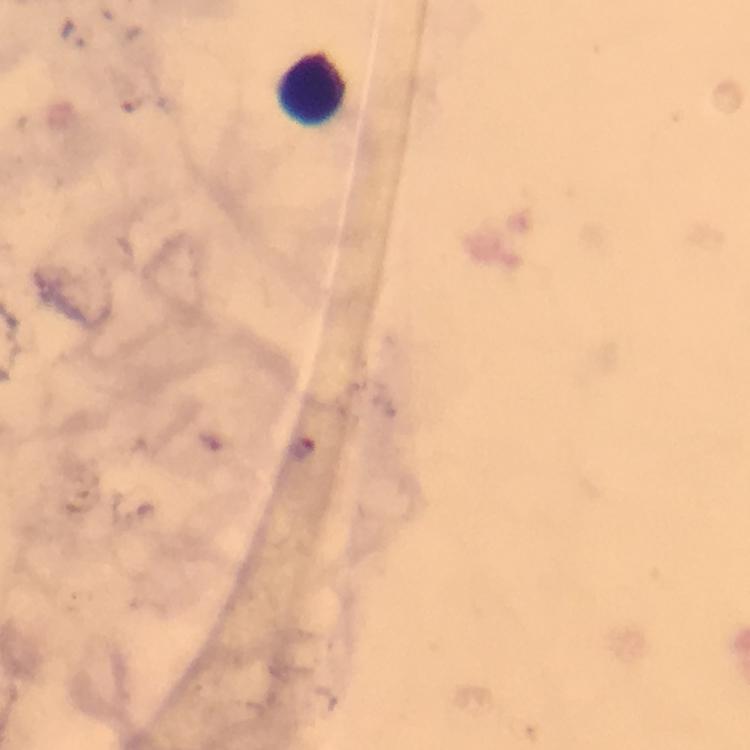
Approximate centers as (x, y) in pixels. Leukocyte locations: (313, 90). At 100x magnification. Malaria parasites: none detected. Photographed through the microscope with a smartphone camera. From a malaria diagnostic workup. Immersion oil was used. Thick blood smear. Giemsa stain. Image is 750×750 pixels. A crop from one field of view.